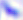

Summary:
  - Modality: micrograph
  - Magnification: 400x
  - Identification: Toxoplasma gondii